Assess this cell for malaria.
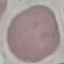
It is uninfected.

image type = automatically extracted cell patch, resized to 64 × 64 pixels
stain = Giemsa
preparation = thin smear
capture = smartphone through the microscope eyepiece